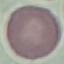

Malaria status: uninfected. Acquired by smartphone through the microscope eyepiece. Thin blood smear. Cell patch, automatically extracted from a larger field of view and resized to 64 × 64 pixels. Giemsa stain.